Assess the morphology of the red blood cells.
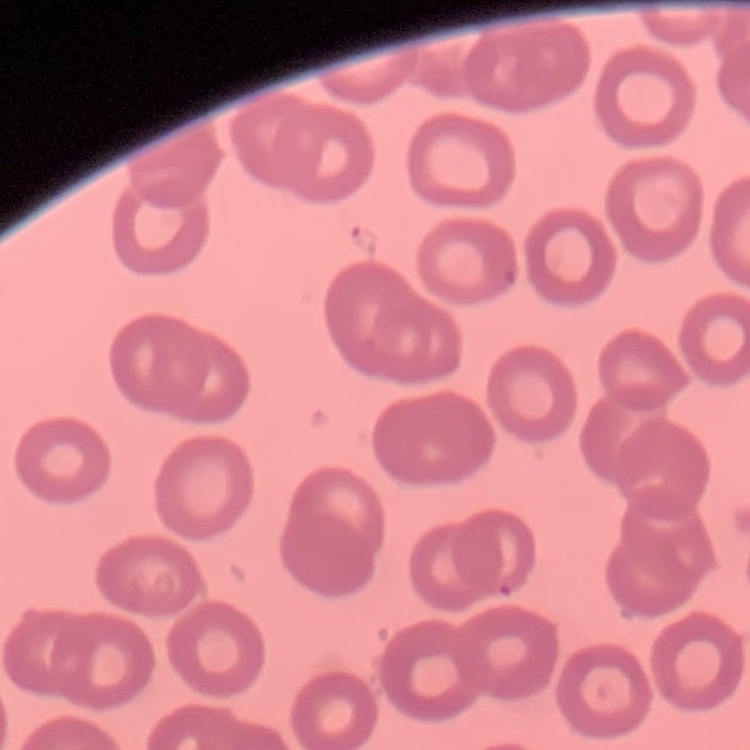

No rouleaux formation.

Stained with either Field's or Giemsa. Thin peripheral smear. Square crop of a larger photomicrograph.